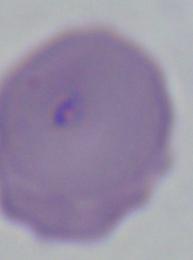 Photomicrograph. A Babesia parasite is shown. 1000x magnification.